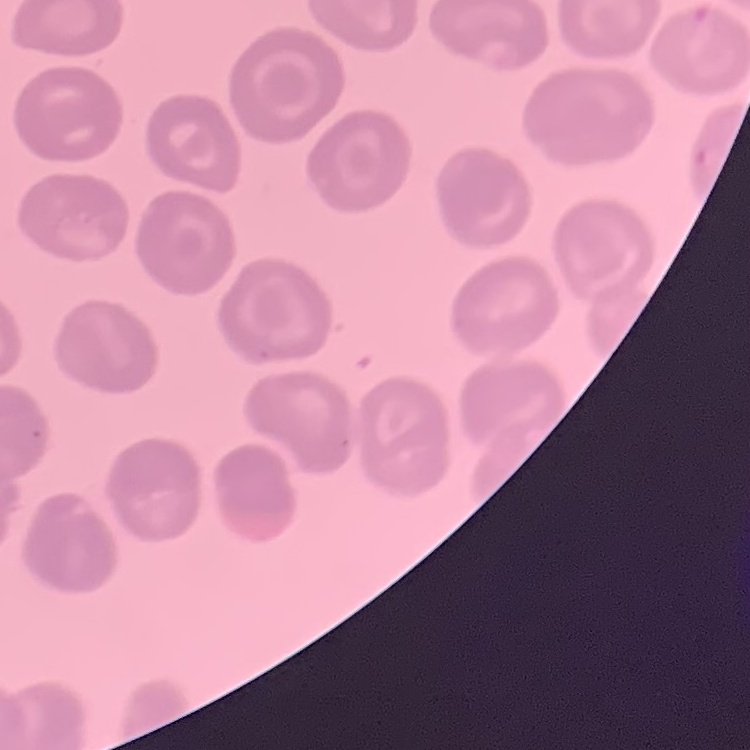
The red blood cells exhibit no rouleaux formation. Thin blood smear. Stained with either Field's or Giemsa. Square crop of a larger photomicrograph.